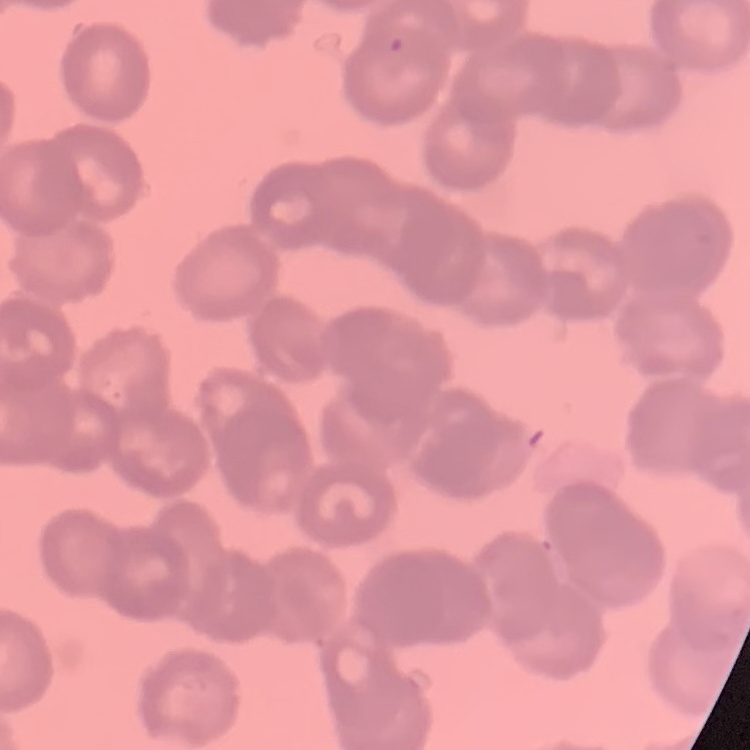

red blood cell morphology = rouleaux formation
preparation = thin blood film
stain = Field's or Giemsa
image type = one tile cut from a larger photomicrograph